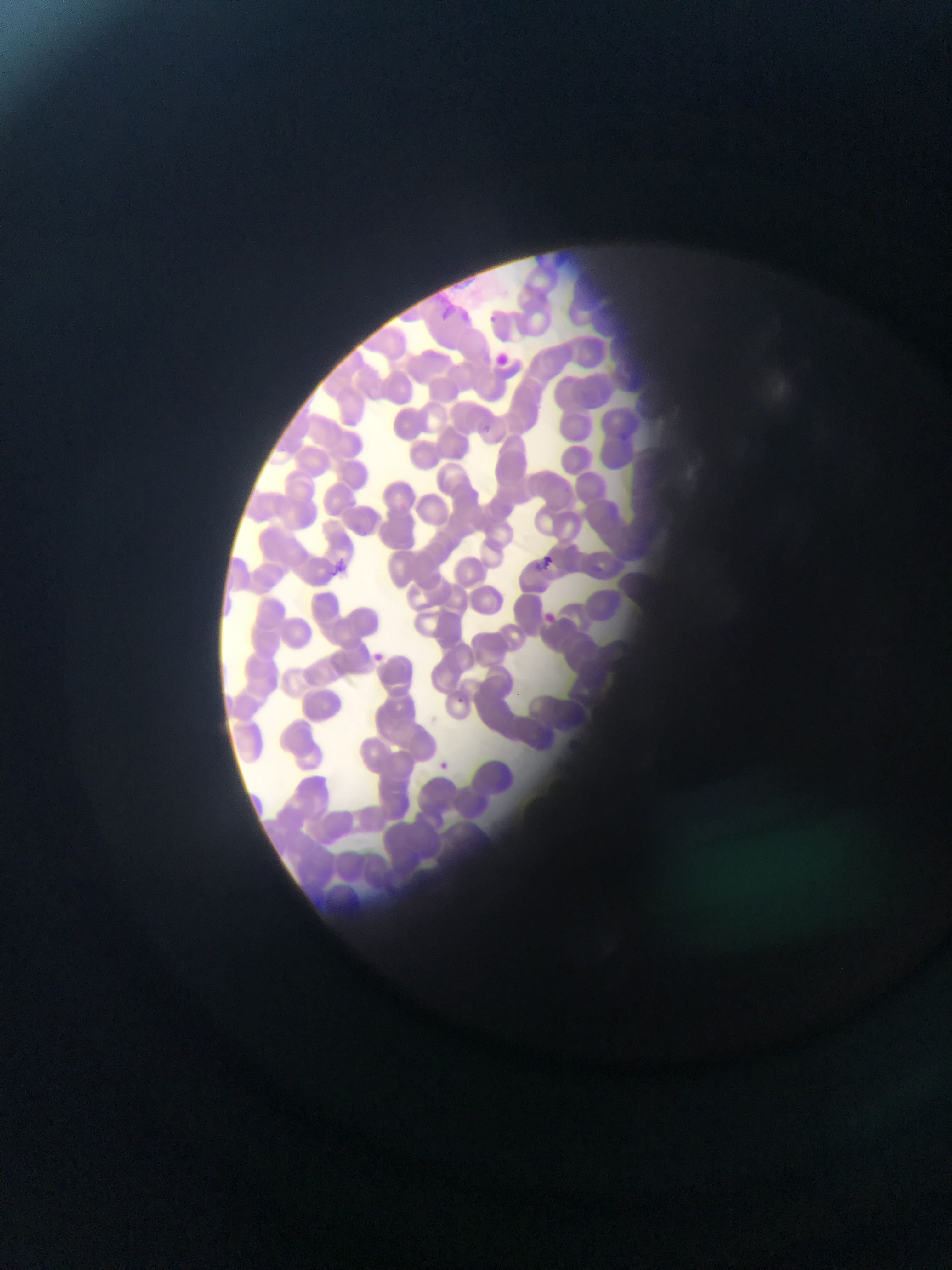
Approximate bounding boxes as (left, top, right, bottom) in pixels. Malaria parasite locations: (441, 301, 457, 318), (491, 309, 504, 320), (475, 419, 499, 436), (536, 543, 556, 569), (333, 555, 350, 578), (538, 606, 559, 623), (456, 686, 469, 704), (440, 757, 457, 771). One field of view. Photographed through a microscope with a mobile-phone camera. Image is 952×1270 pixels. Sample from Ghana. Thin blood film.